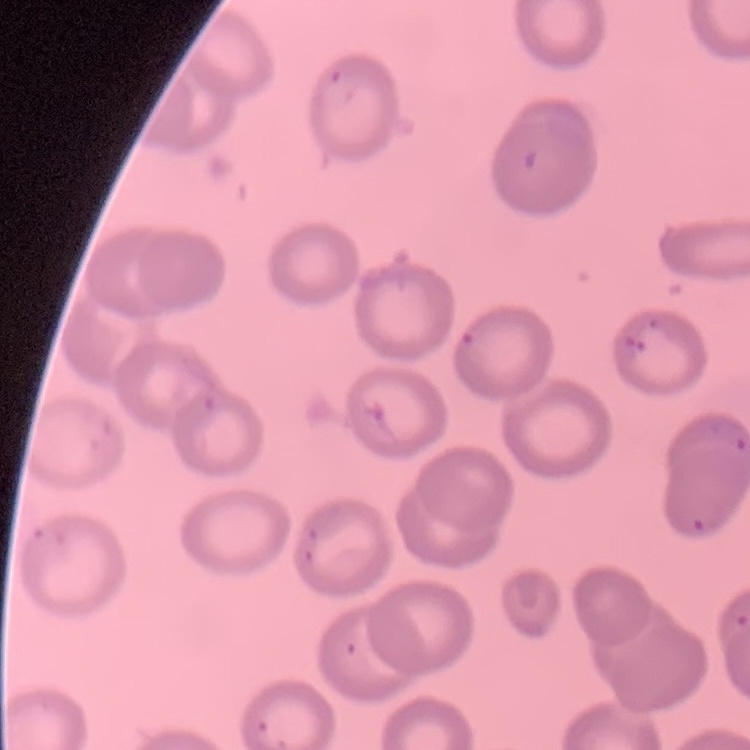
The erythrocytes show no rouleaux formation. One tile cut from a larger photomicrograph. Thin peripheral smear. Stained with either Field's or Giemsa.